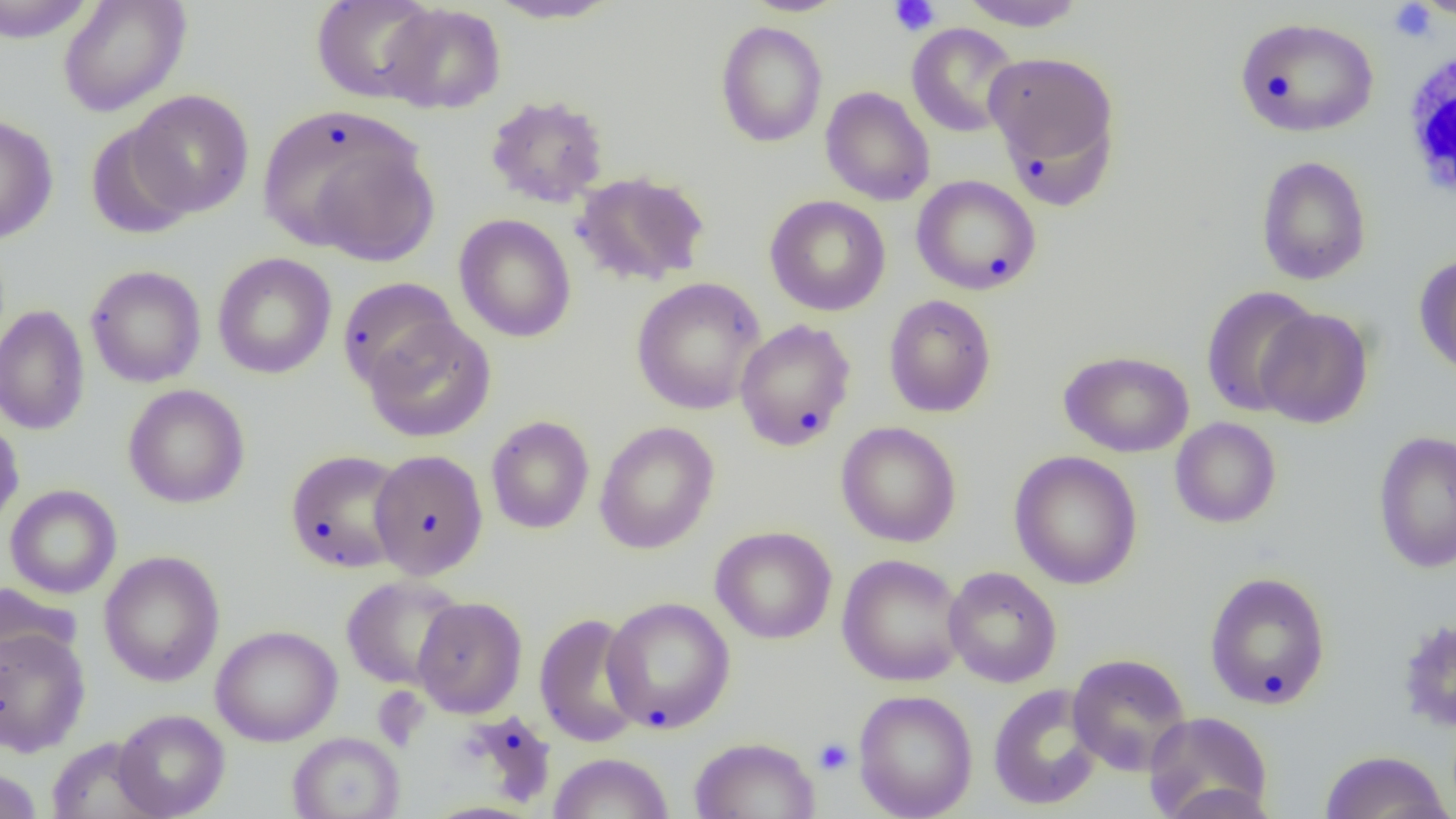
Approximate bounding boxes as (x1,y1)-(x2,y2) corner pairs in pixels. Uninfected red blood cell locations: (0,0)-(97,43), (58,0)-(191,117), (311,0)-(441,104), (740,0)-(851,17), (957,0)-(1087,30), (1412,0)-(1455,21), (485,1)-(623,24), (380,3)-(506,114), (1235,17)-(1379,138), (715,20)-(828,148), (906,23)-(1021,138), (984,51)-(1120,180), (820,86)-(935,206), (127,90)-(255,217), (485,94)-(610,208), (257,104)-(434,261), (0,113)-(59,245), (85,122)-(197,240), (1256,155)-(1371,285), (571,171)-(710,288), (911,175)-(1042,295), (765,195)-(891,316), (454,213)-(576,342), (212,252)-(337,379), (1414,254)-(1456,380), (85,264)-(206,388), (338,277)-(460,392), (630,277)-(766,415), (1201,285)-(1320,417), (883,294)-(997,418), (0,304)-(91,436), (1256,308)-(1373,429), (362,316)-(496,443), (734,318)-(857,451), (1059,349)-(1194,458), (123,384)-(250,508), (0,414)-(24,532), (486,415)-(594,534), (1170,417)-(1282,528), (836,421)-(962,547), (594,422)-(720,554), (1372,430)-(1456,573), (285,449)-(410,574), (369,449)-(488,580), (1009,450)-(1142,590), (5,484)-(122,599), (710,525)-(837,644), (99,550)-(225,687), (837,553)-(967,686), (944,566)-(1062,688), (1204,571)-(1332,710), (341,575)-(467,690), (0,581)-(83,673), (413,596)-(527,717), (602,596)-(736,734), (534,612)-(647,747), (1398,618)-(1456,734), (211,624)-(343,746), (0,627)-(91,757), (1067,653)-(1191,776), (988,683)-(1104,811), (853,689)-(978,819), (112,709)-(230,818), (1142,711)-(1274,819), (288,731)-(405,819), (45,736)-(164,819), (689,736)-(820,819), (1319,750)-(1452,819), (549,752)-(674,818), (0,767)-(43,819), (1155,783)-(1282,819). Platelet locations: (888,0)-(941,36), (1388,2)-(1437,42), (813,738)-(854,775). White blood cell locations: (1399,41)-(1455,208). Slide-level diagnosis: negative for blood parasites. 1000x magnification. Light microscopy. Image is 1456×819 pixels. One field of a larger specimen. Thin blood film.